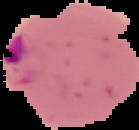
Summary:
  - Image size: 139×130 pixels
  - Result: Plasmodium parasites identified
  - Preparation: thin blood film
  - Image type: segmented cell region with the area outside set to black